Identify the blood parasite species.
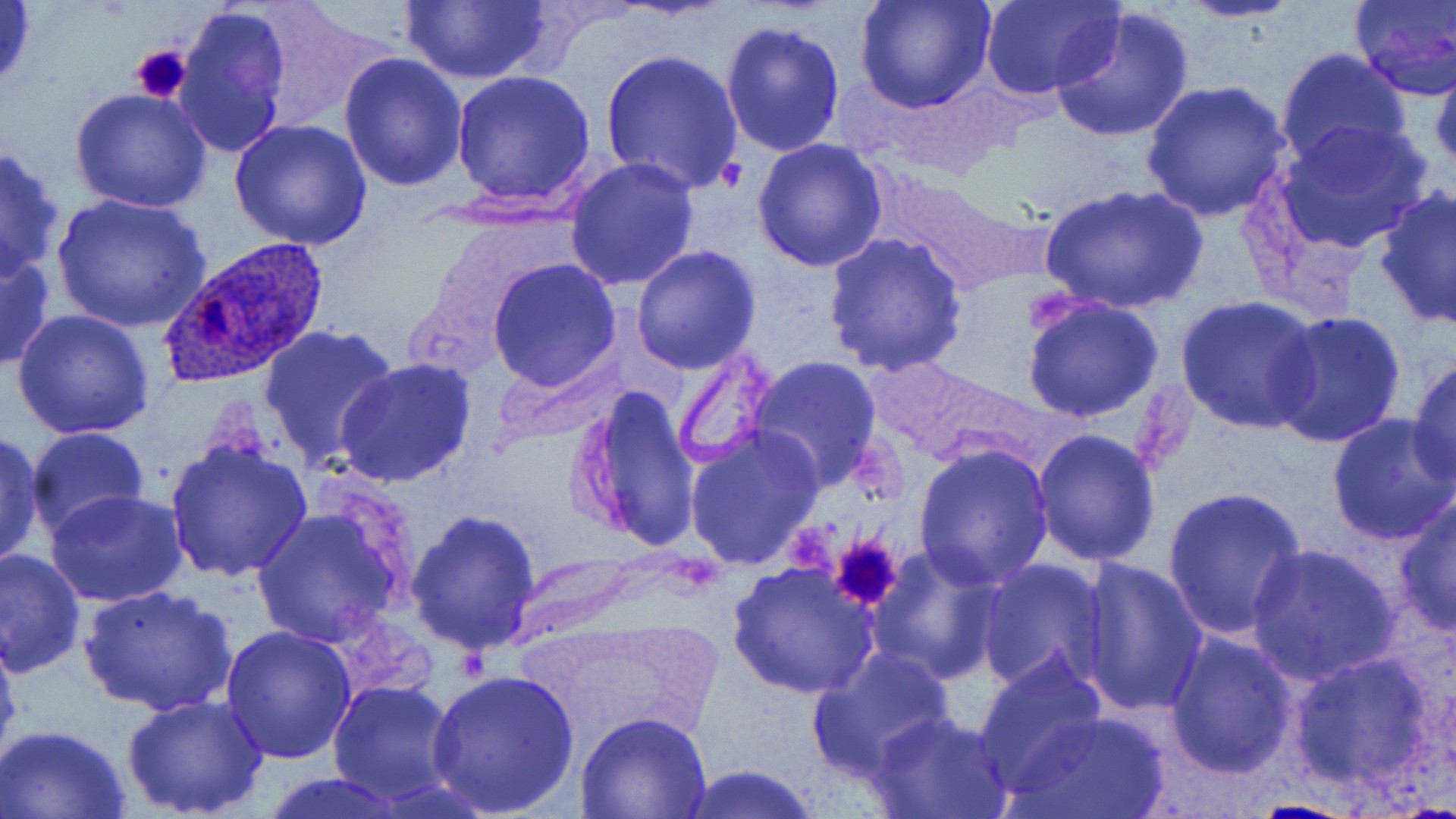
Plasmodium ovale.

Approximate bounding boxes as (x1, y1, x2, y2) in pixels. Platelet locations: (130, 44, 191, 104), (827, 533, 905, 612). Plasmodium ovale-infected red blood cell locations: (160, 237, 332, 387). Uninfected red blood cell locations: (246, 0, 394, 130), (397, 0, 556, 86), (980, 0, 1124, 100), (1176, 0, 1304, 24), (1348, 0, 1456, 100), (0, 1, 39, 98), (857, 1, 993, 113), (174, 4, 293, 158), (1050, 6, 1196, 145), (721, 20, 847, 158), (1275, 48, 1413, 172), (601, 49, 743, 194), (339, 53, 470, 193), (1429, 53, 1455, 173), (452, 73, 596, 209), (1139, 80, 1293, 222), (70, 88, 212, 213), (228, 118, 373, 250), (1274, 120, 1436, 255), (754, 137, 888, 271), (0, 145, 66, 282), (564, 156, 699, 290), (871, 168, 1035, 296), (1038, 183, 1205, 316), (1375, 186, 1456, 329), (50, 192, 212, 333), (424, 213, 575, 327), (824, 233, 968, 377), (0, 244, 54, 373), (631, 245, 761, 374), (488, 258, 622, 392), (1177, 295, 1324, 434), (1021, 296, 1165, 424), (11, 309, 156, 441), (1268, 310, 1405, 449), (259, 320, 400, 472), (670, 343, 779, 471), (499, 351, 630, 444), (747, 354, 884, 488), (1408, 356, 1455, 489), (334, 357, 479, 488), (572, 385, 702, 554), (1326, 411, 1456, 544), (24, 427, 149, 541), (685, 427, 824, 572), (1031, 428, 1162, 569), (0, 431, 45, 569), (164, 436, 314, 585), (912, 443, 1055, 590), (1162, 486, 1306, 640), (44, 491, 189, 608), (1393, 494, 1455, 637), (251, 507, 406, 646), (407, 511, 543, 653), (1246, 543, 1401, 684), (866, 548, 1007, 686), (1, 549, 87, 682), (977, 558, 1109, 694), (1076, 558, 1209, 716), (727, 561, 880, 699), (80, 585, 237, 720), (0, 622, 23, 770), (220, 625, 356, 764), (1165, 631, 1299, 778), (806, 646, 957, 782), (1286, 648, 1443, 795), (973, 654, 1108, 793), (426, 671, 579, 816), (329, 680, 459, 805), (121, 693, 270, 817), (867, 709, 1014, 819), (1001, 710, 1169, 819), (574, 712, 714, 819), (0, 725, 131, 818), (675, 764, 823, 819), (254, 775, 413, 819). Light microscopy. Single field of view. Captured at 1000x magnification. Image is 1456×819 pixels. Thin blood smear. May-Grünwald-Giemsa stain.